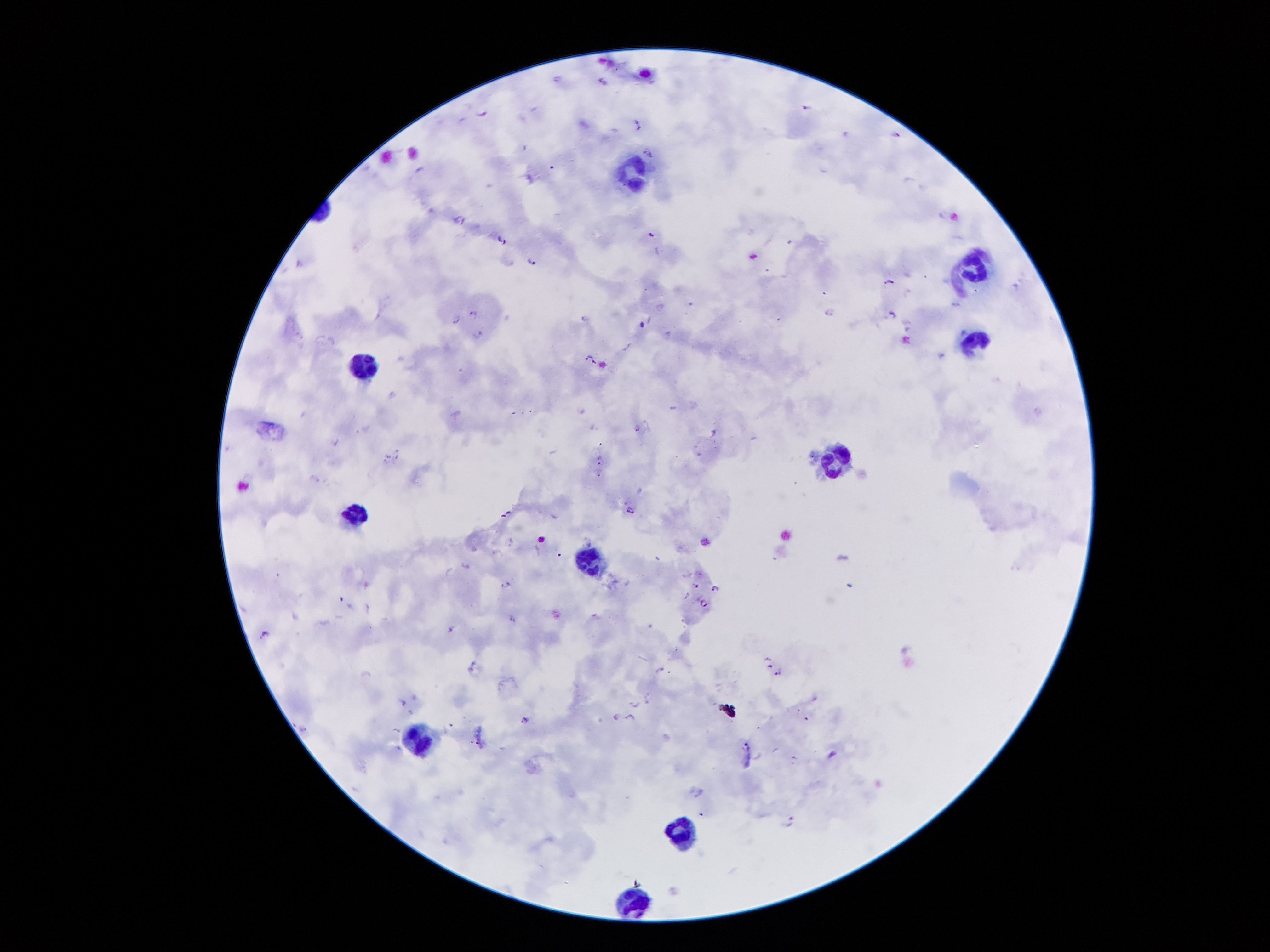
Approximate centers as {x, y} in pixels.
Summary:
  - Leukocyte locations: {632, 171}, {973, 267}, {973, 336}, {365, 366}, {833, 459}, {355, 514}, {592, 562}, {419, 738}, {679, 832}, {629, 900}
  - Malaria parasite locations: {602, 80}, {804, 105}, {481, 110}, {636, 123}, {897, 132}, {523, 146}, {646, 148}, {527, 175}, {458, 217}, {649, 233}, {501, 238}, {533, 257}, {888, 282}, {1015, 286}, {661, 307}, {471, 310}, {889, 311}, {454, 317}, {584, 317}, {906, 323}, {476, 332}, {627, 346}, {941, 354}, {590, 356}, {390, 392}, {635, 427}, {335, 442}, {386, 455}, {396, 455}, {598, 458}, {598, 471}, {630, 509}, {506, 514}, {509, 542}, {464, 565}, {506, 583}, {697, 584}, {715, 587}, {340, 597}, {702, 601}, {367, 607}, {296, 616}, {512, 617}, {451, 627}, {264, 632}, {766, 658}, {659, 669}, {777, 671}, {646, 698}, {403, 702}, {635, 704}, {407, 710}, {616, 715}, {628, 716}, {525, 719}, {793, 757}, {698, 791}, {791, 819}
  - Image size: 1270×952 pixels
  - Patient malaria status: positive for Plasmodium falciparum
  - Field of view: one from this slide
  - Stain: Giemsa
  - Preparation: thick blood film
  - Capture: smartphone camera through the microscope eyepiece
  - Magnification: 100x